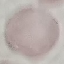
Result: negative for malaria parasites. Giemsa stain. Automatically extracted cell patch, resized to 64 × 64 pixels. Acquired by smartphone through the microscope eyepiece. Thin blood smear.